Report the malaria status of this cell.
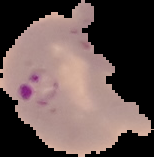
Parasitized.

Summary:
  - Image type: segmented cell region with the area outside set to black
  - Image size: 154×157 pixels
  - Preparation: thin blood film